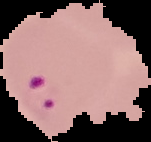
The area outside the segmented cell region is set to black. Image is 151×142 pixels. Result: Plasmodium parasites detected. From a thin blood film.